State the preparation type.
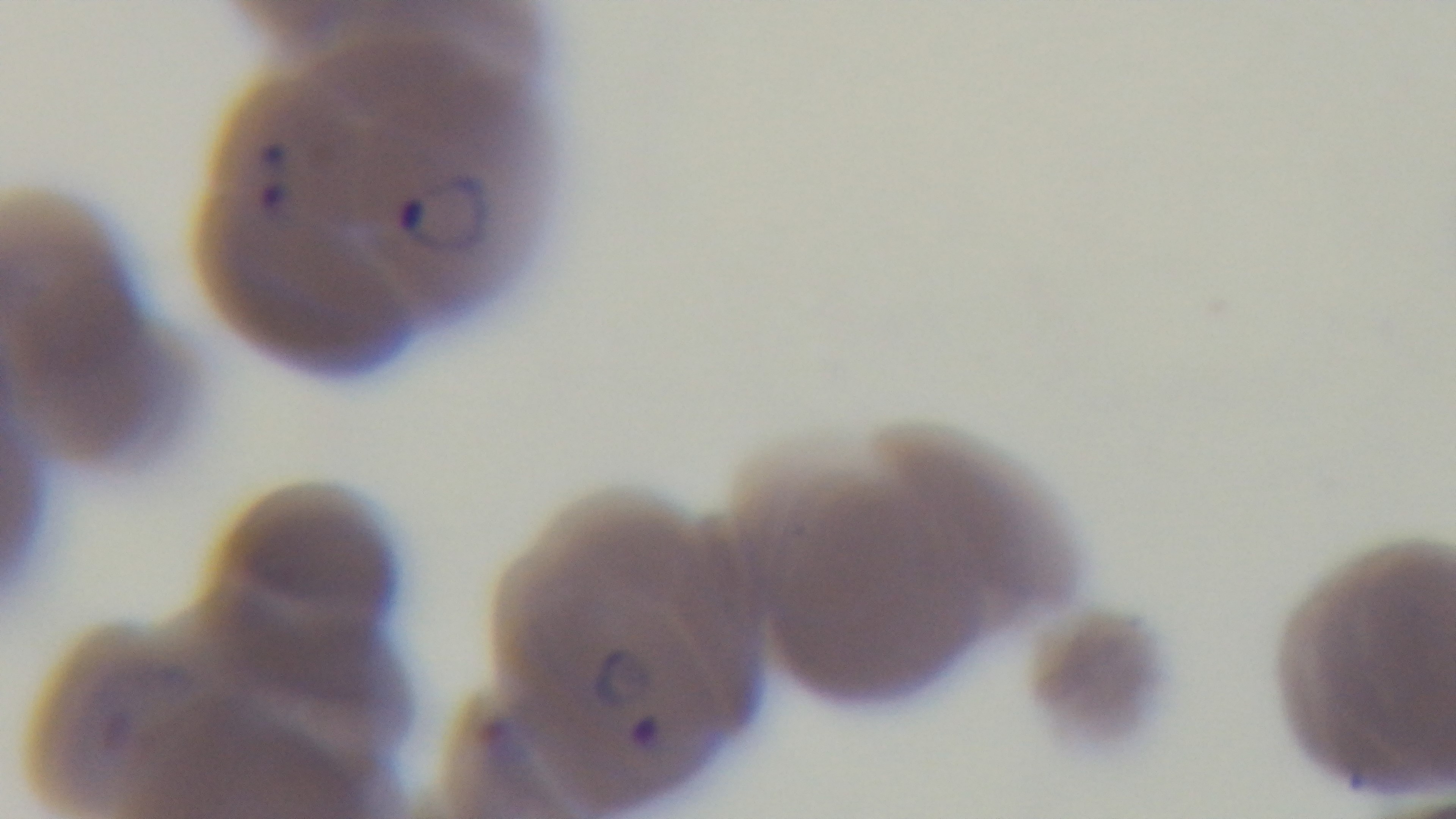
It is a thin blood film.

{
  "capture": "mounted 4K digital camera",
  "malaria_status": "infected",
  "objective": "100x oil immersion",
  "modality": "light microscopy",
  "stain": "Giemsa",
  "field_of_view": "one from the slide"
}